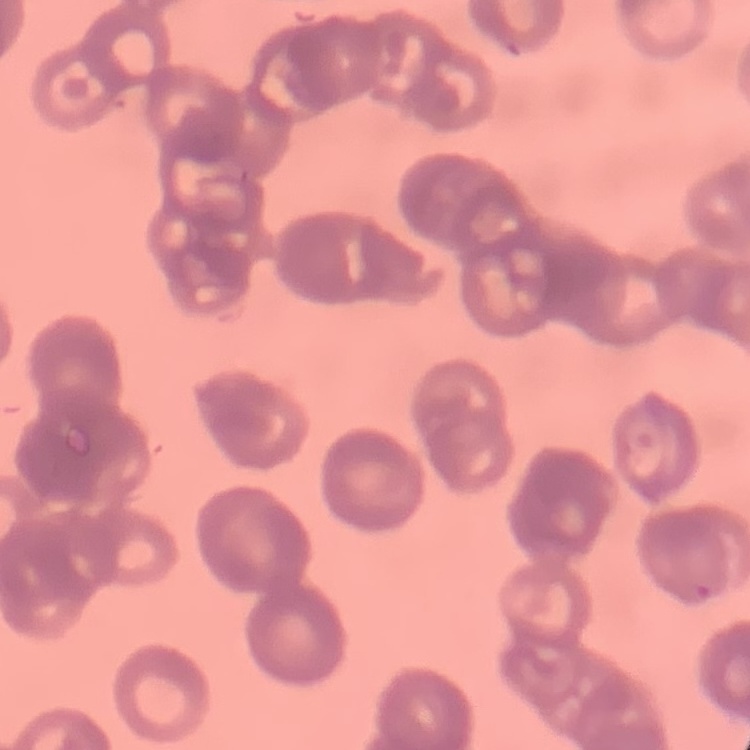
Summary:
  - Red blood cell morphology: rouleaux formation
  - Preparation: thin peripheral smear
  - Stain: Field's or Giemsa
  - Image type: one tile cut from a larger photomicrograph